Classify this cell by malaria status.
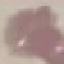
Uninfected.

Summary:
  - Stain: Giemsa
  - Image type: automatically extracted cell patch, resized to 64 × 64 pixels
  - Capture: smartphone camera at the microscope eyepiece
  - Preparation: thin smear